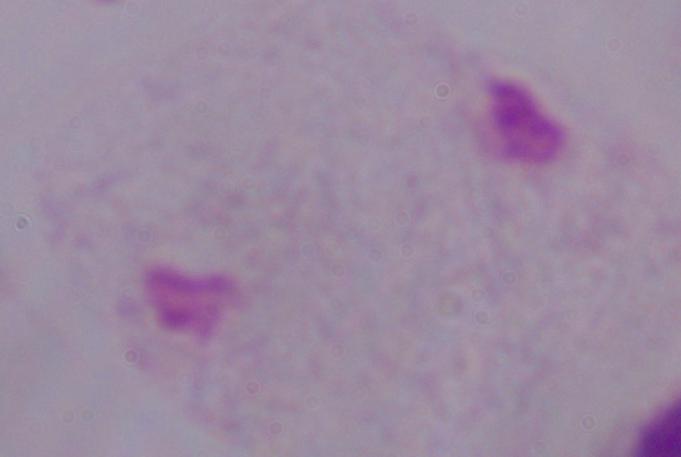

Summary:
  - Modality: photomicrograph
  - Magnification: 1000x
  - Identification: trichomonad